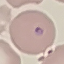
Result: malaria parasites detected. Automatically extracted cell patch, resized to 64 × 64 pixels. Thin blood film. Giemsa-stained preparation. Photographed with a smartphone camera at the microscope eyepiece.